Locate and identify every blood parasite.
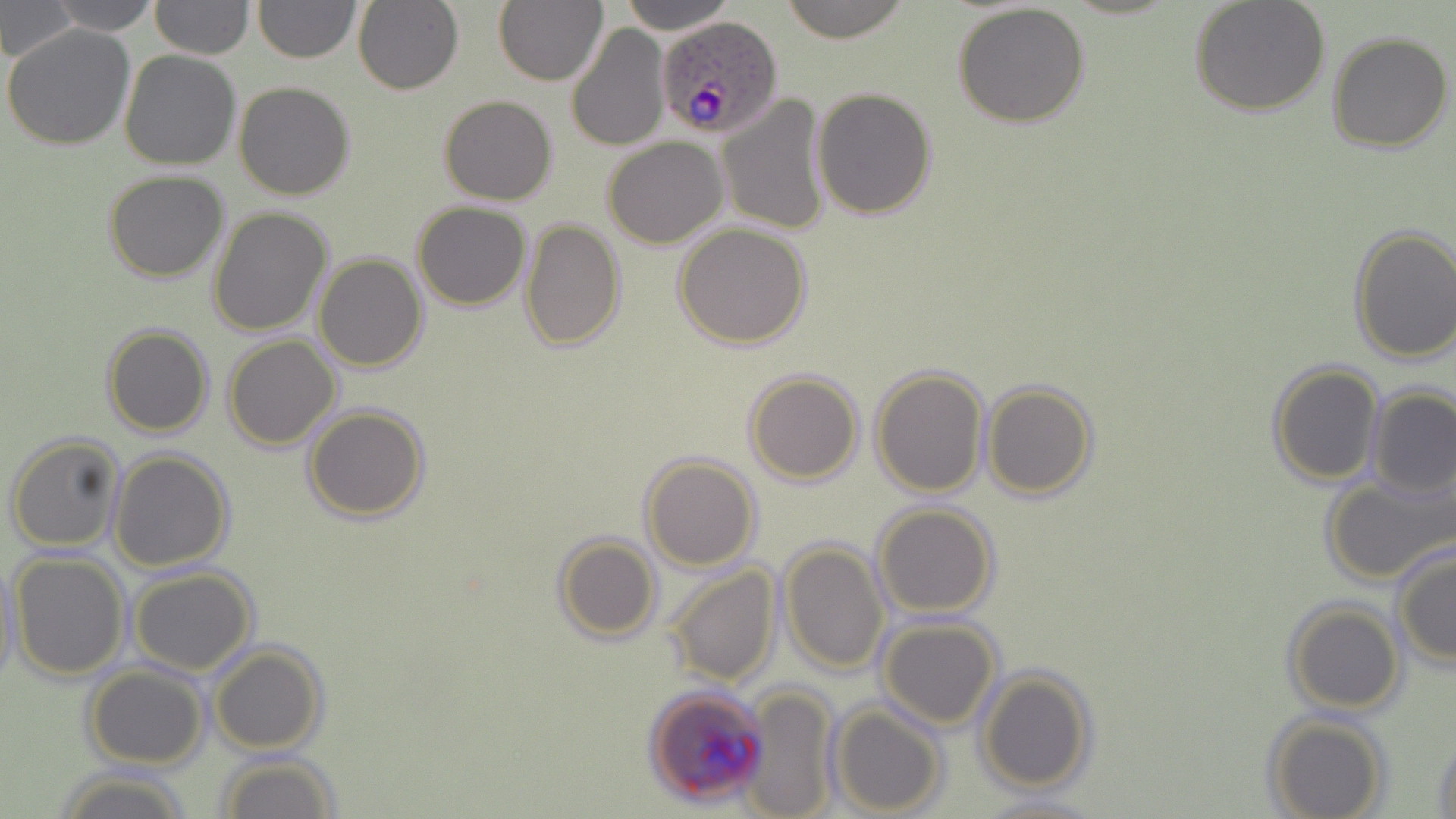

Approximate bounding boxes as [x1, y1, x2, y2] in pixels.
Plasmodium ovale-infected red blood cells: [655, 16, 783, 140].
No Plasmodium falciparum, Plasmodium malariae, Plasmodium vivax, Babesia divergens, or Trypanosoma brucei observed.

Uninfected red blood cell locations: [1, 0, 77, 62], [149, 0, 253, 58], [253, 0, 360, 63], [496, 0, 609, 88], [618, 0, 736, 34], [776, 0, 916, 43], [1188, 0, 1332, 118], [43, 1, 163, 33], [354, 1, 463, 96], [952, 2, 1090, 128], [2, 22, 136, 151], [565, 23, 671, 152], [1326, 30, 1454, 153], [118, 49, 240, 170], [234, 82, 354, 201], [812, 86, 939, 220], [716, 92, 831, 237], [440, 95, 556, 206], [603, 137, 728, 249], [102, 171, 230, 282], [411, 203, 530, 312], [207, 206, 332, 337], [519, 219, 627, 354], [674, 223, 812, 351], [1348, 225, 1456, 365], [314, 252, 428, 372], [101, 323, 215, 438], [224, 335, 342, 451], [1266, 360, 1384, 485], [870, 365, 991, 499], [744, 370, 864, 485], [980, 382, 1099, 499], [1365, 388, 1456, 500], [302, 404, 430, 522], [7, 433, 126, 553], [107, 449, 235, 571], [641, 454, 761, 571], [1320, 469, 1454, 586], [874, 502, 998, 618], [553, 534, 662, 645], [779, 540, 891, 675], [1391, 544, 1455, 668], [9, 552, 129, 681], [1, 557, 22, 689], [661, 562, 781, 686], [129, 566, 259, 675], [1283, 600, 1403, 715], [878, 617, 1002, 729], [209, 644, 327, 753], [83, 664, 210, 768], [975, 667, 1096, 793], [736, 683, 841, 819], [829, 704, 946, 817], [1264, 714, 1390, 819], [1430, 733, 1455, 818], [213, 751, 343, 819], [55, 767, 193, 819], [976, 795, 1106, 819]. Slide-level diagnosis: Plasmodium ovale. Image is 1456×819 pixels. 1000x magnification. One field of a larger specimen. Thin blood film. May-Grünwald-Giemsa-stained preparation. Light microscopy.